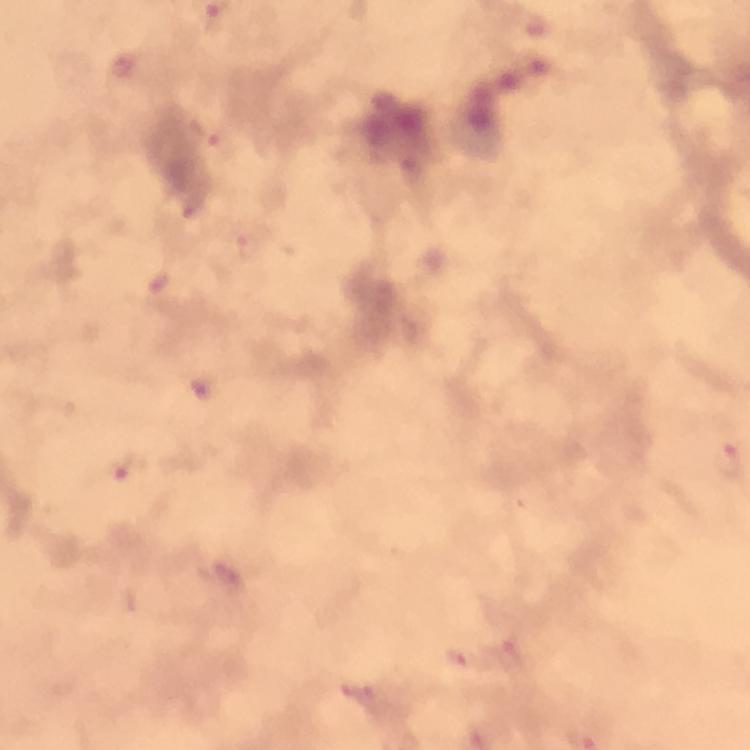

Approximate centers as {x, y} in pixels.
Summary:
  - Malaria parasite locations: {209, 137}, {247, 245}, {729, 463}, {127, 467}, {508, 652}, {460, 657}, {359, 692}
  - Cropped from: one field of view
  - Capture: smartphone camera through the microscope
  - Stain: Giemsa
  - Context: from a malaria diagnostic workup
  - Magnification: 100x
  - Image size: 750×750 pixels
  - Preparation: thick blood smear
  - Immersion oil: applied